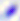

Summary:
  - Identification: Toxoplasma gondii
  - Modality: micrograph
  - Magnification: 400x